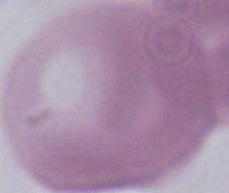
Summary:
  - Magnification: 1000x
  - Identification: red blood cell
  - Modality: micrograph